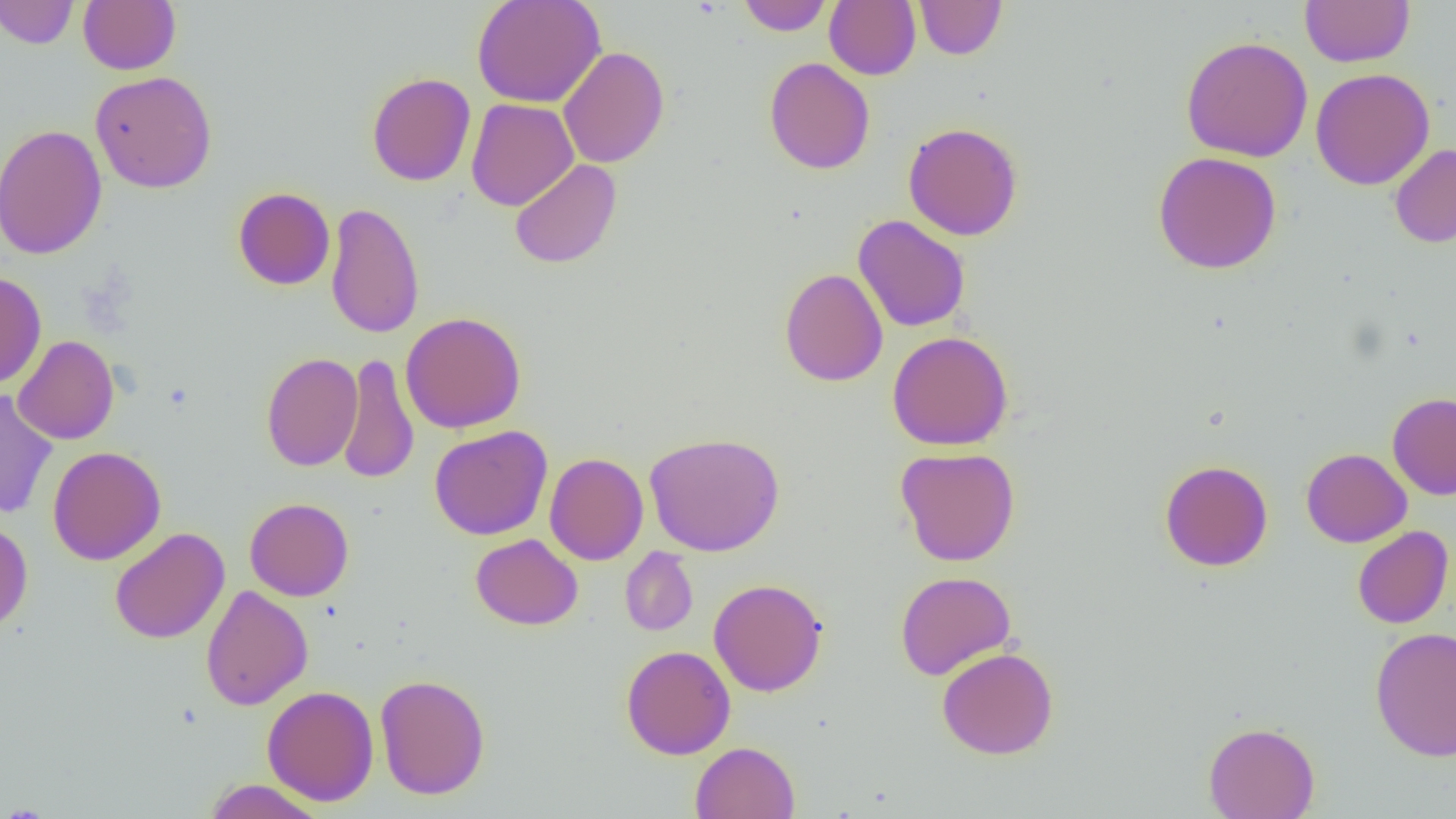
slide_level_diagnosis: negative for blood parasites
modality: optical microscopy
magnification: 1000x
image_size: 1456×819 pixels
uninfected_red_blood_cell_locations: 'approximate bounding boxes as named x1/y1/x2/y2 corners in pixels: (x1=0, y1=0, x2=79, y2=49), (x1=78, y1=0, x2=181, y2=75), (x1=472, y1=0, x2=606, y2=109), (x1=737, y1=0, x2=833, y2=35), (x1=825, y1=0, x2=920, y2=80), (x1=914, y1=0, x2=1007, y2=60), (x1=1300, y1=0, x2=1415, y2=67), (x1=1180, y1=35, x2=1313, y2=162), (x1=558, y1=47, x2=669, y2=168), (x1=764, y1=57, x2=875, y2=175), (x1=1310, y1=67, x2=1435, y2=190), (x1=90, y1=70, x2=217, y2=193), (x1=366, y1=72, x2=476, y2=186), (x1=466, y1=98, x2=578, y2=211), (x1=903, y1=122, x2=1023, y2=241), (x1=0, y1=124, x2=108, y2=260), (x1=1389, y1=143, x2=1456, y2=248), (x1=1152, y1=151, x2=1282, y2=274), (x1=509, y1=159, x2=622, y2=269), (x1=233, y1=187, x2=335, y2=290), (x1=325, y1=202, x2=425, y2=339), (x1=853, y1=214, x2=971, y2=333), (x1=779, y1=267, x2=888, y2=387), (x1=0, y1=271, x2=47, y2=389), (x1=400, y1=311, x2=526, y2=433), (x1=887, y1=331, x2=1014, y2=451), (x1=13, y1=335, x2=119, y2=445), (x1=261, y1=352, x2=363, y2=472), (x1=337, y1=354, x2=420, y2=485), (x1=0, y1=390, x2=58, y2=520), (x1=1387, y1=392, x2=1456, y2=500), (x1=429, y1=425, x2=553, y2=540), (x1=644, y1=432, x2=785, y2=556), (x1=47, y1=446, x2=166, y2=565), (x1=895, y1=446, x2=1021, y2=566), (x1=1301, y1=448, x2=1412, y2=547), (x1=544, y1=452, x2=648, y2=565), (x1=1159, y1=459, x2=1274, y2=571), (x1=244, y1=497, x2=354, y2=601), (x1=0, y1=520, x2=33, y2=632), (x1=1352, y1=526, x2=1454, y2=629), (x1=109, y1=527, x2=230, y2=643), (x1=471, y1=533, x2=583, y2=630), (x1=620, y1=547, x2=698, y2=636), (x1=895, y1=571, x2=1016, y2=680), (x1=709, y1=578, x2=828, y2=697), (x1=200, y1=584, x2=313, y2=711), (x1=1370, y1=626, x2=1456, y2=761), (x1=621, y1=645, x2=735, y2=759), (x1=936, y1=646, x2=1059, y2=760), (x1=374, y1=673, x2=491, y2=800), (x1=262, y1=685, x2=379, y2=806), (x1=1203, y1=721, x2=1320, y2=819), (x1=690, y1=741, x2=800, y2=818), (x1=203, y1=779, x2=327, y2=819)'
preparation: thin blood film
field_of_view: single